Locate every Plasmodium falciparum-infected red blood cell.
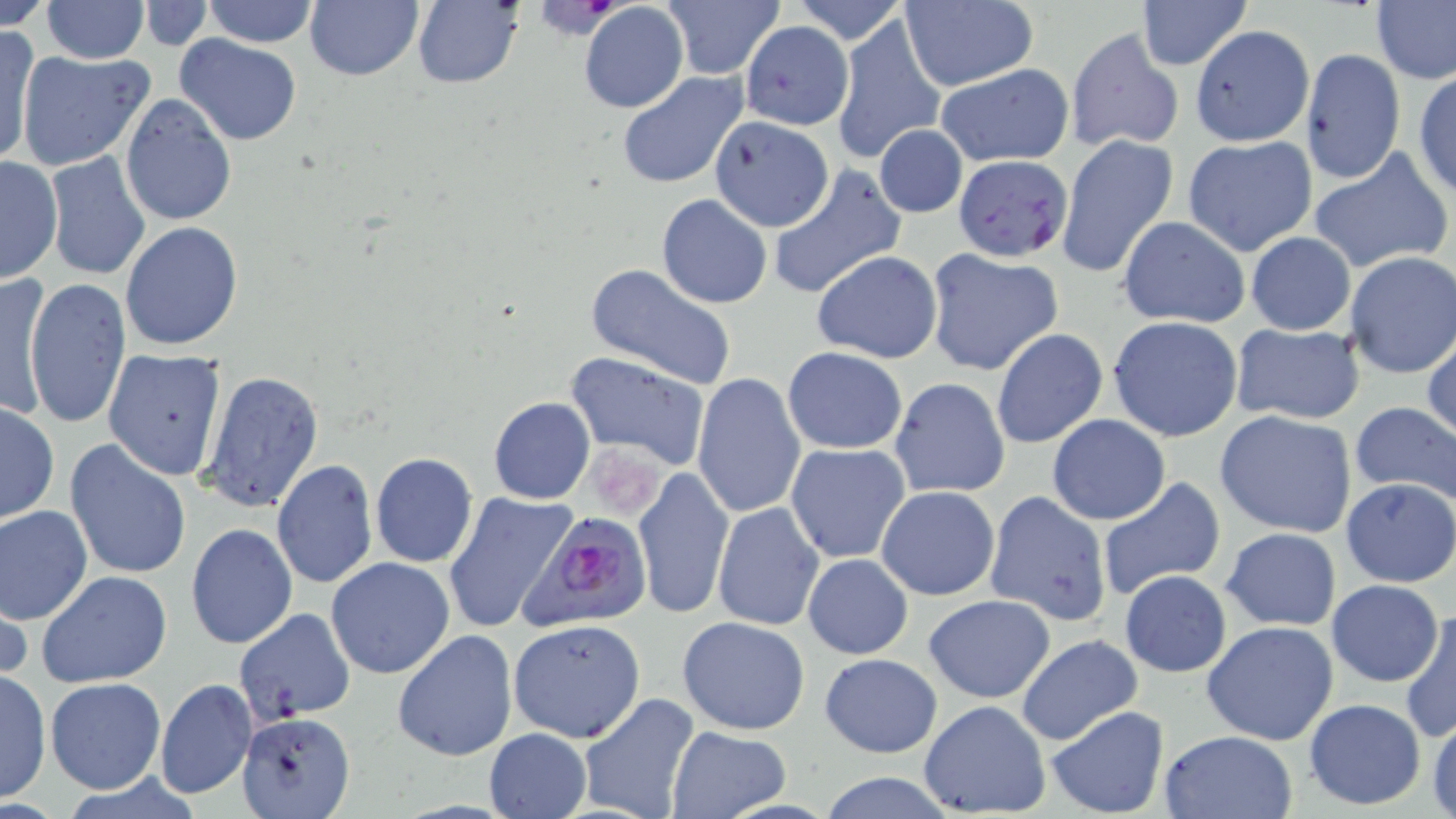

Approximate bounding boxes as (x1, y1, x2, y2) in pixels.
Plasmodium falciparum-infected red blood cells: (516, 510, 653, 632).

Summary:
  - Uninfected red blood cell locations: (2, 0, 56, 31), (43, 0, 147, 63), (199, 0, 320, 48), (303, 0, 424, 81), (408, 0, 525, 91), (791, 0, 910, 45), (1136, 0, 1251, 71), (1371, 0, 1455, 86), (661, 1, 786, 80), (140, 2, 215, 48), (900, 2, 1038, 91), (578, 3, 688, 114), (832, 13, 943, 165), (740, 21, 853, 131), (1192, 24, 1314, 144), (1, 25, 37, 166), (1064, 29, 1185, 154), (175, 35, 302, 145), (1300, 49, 1404, 183), (17, 50, 155, 171), (935, 65, 1074, 167), (1413, 69, 1455, 198), (617, 71, 748, 190), (118, 93, 237, 226), (708, 117, 834, 232), (874, 124, 968, 219), (1181, 134, 1318, 257), (1056, 135, 1178, 280), (1307, 149, 1452, 273), (45, 151, 151, 280), (0, 155, 63, 283), (953, 155, 1074, 261), (767, 167, 905, 298), (656, 193, 773, 308), (1118, 215, 1250, 328), (119, 221, 244, 352), (1245, 232, 1356, 336), (812, 249, 943, 363), (925, 249, 1062, 376), (1344, 251, 1456, 378), (585, 263, 740, 392), (2, 273, 50, 422), (23, 278, 131, 429), (1106, 315, 1244, 442), (1229, 321, 1366, 424), (989, 327, 1107, 449), (1423, 328, 1456, 446), (782, 346, 908, 454), (103, 348, 228, 480), (564, 351, 710, 469), (198, 371, 324, 513), (692, 373, 806, 519), (890, 376, 1010, 498), (487, 396, 597, 504), (1348, 399, 1456, 505), (1, 402, 60, 523), (1213, 409, 1358, 538), (1046, 414, 1171, 525), (64, 439, 192, 580), (785, 443, 909, 564), (369, 452, 478, 568), (271, 459, 377, 589), (633, 467, 733, 621), (1095, 477, 1225, 601), (1341, 477, 1456, 588), (876, 484, 1000, 600), (984, 490, 1113, 627), (444, 492, 577, 635), (712, 502, 825, 632), (0, 504, 93, 625), (186, 523, 297, 649), (1220, 527, 1342, 632), (802, 553, 913, 660), (326, 557, 456, 679), (1118, 570, 1232, 677), (36, 571, 172, 689), (1, 579, 31, 687), (1327, 579, 1443, 687), (923, 595, 1055, 704), (1400, 604, 1456, 742), (234, 607, 356, 723), (677, 615, 810, 735), (508, 618, 646, 743), (1202, 621, 1339, 746), (392, 629, 519, 761), (1016, 635, 1143, 746), (818, 652, 943, 759), (0, 669, 51, 803), (45, 677, 166, 794), (156, 679, 256, 799), (578, 693, 700, 819), (1303, 697, 1427, 811), (919, 699, 1050, 817), (1045, 706, 1169, 817), (237, 710, 356, 817), (1427, 710, 1456, 819), (666, 726, 793, 817), (483, 728, 592, 819), (1159, 730, 1297, 818), (818, 773, 959, 818)
  - Slide-level diagnosis: Plasmodium falciparum
  - Stain: May-Grünwald-Giemsa
  - Modality: light microscopy
  - Image size: 1456×819 pixels
  - Preparation: thin blood smear
  - Field of view: one of a larger specimen
  - Magnification: 1000x